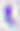

Micrograph. Toxoplasma gondii is seen. Captured at 400x magnification.